Name the cell type shown.
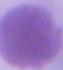

This is an erythrocyte.

Micrograph. Captured at 1000x magnification.